Locate every uninfected red blood cell.
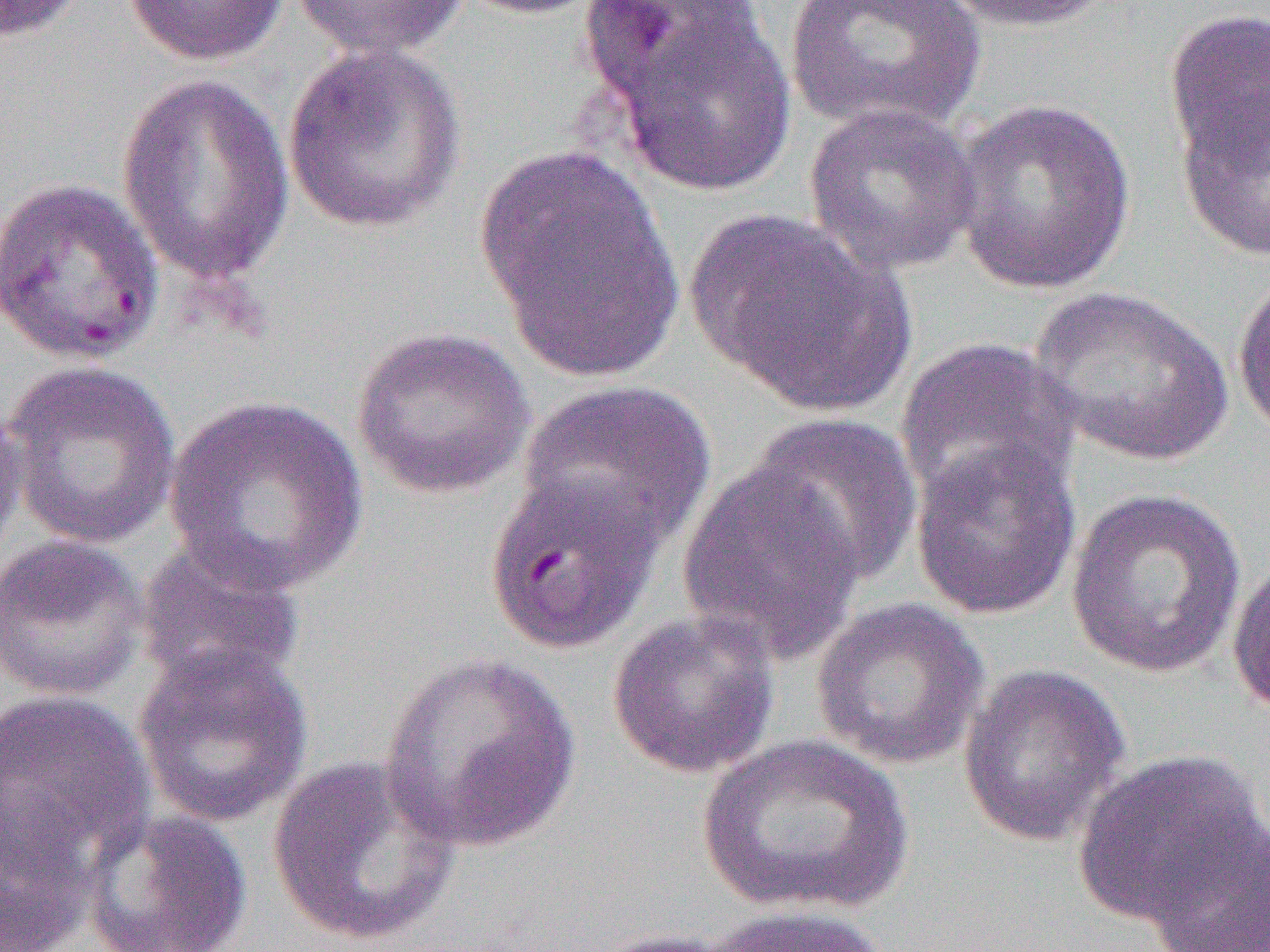

Approximate bounding boxes as named x1/y1/x2/y2 corners in pixels.
Uninfected red blood cells: (x1=0, y1=0, x2=92, y2=44), (x1=121, y1=0, x2=290, y2=66), (x1=292, y1=0, x2=469, y2=61), (x1=451, y1=0, x2=612, y2=19), (x1=782, y1=0, x2=987, y2=137), (x1=937, y1=0, x2=1119, y2=34), (x1=579, y1=1, x2=773, y2=104), (x1=591, y1=5, x2=799, y2=195), (x1=1163, y1=6, x2=1270, y2=192), (x1=283, y1=43, x2=467, y2=234), (x1=116, y1=73, x2=295, y2=287), (x1=1173, y1=77, x2=1270, y2=268), (x1=950, y1=98, x2=1137, y2=295), (x1=803, y1=101, x2=982, y2=275), (x1=476, y1=145, x2=683, y2=380), (x1=0, y1=176, x2=165, y2=365), (x1=686, y1=209, x2=908, y2=414), (x1=1233, y1=268, x2=1270, y2=444), (x1=1028, y1=285, x2=1234, y2=467), (x1=350, y1=326, x2=537, y2=500), (x1=894, y1=337, x2=1082, y2=511), (x1=2, y1=359, x2=181, y2=549), (x1=516, y1=377, x2=716, y2=554), (x1=163, y1=393, x2=369, y2=597), (x1=0, y1=395, x2=28, y2=567), (x1=746, y1=411, x2=924, y2=587), (x1=910, y1=436, x2=1081, y2=621), (x1=675, y1=459, x2=867, y2=666), (x1=483, y1=470, x2=664, y2=656), (x1=1065, y1=487, x2=1248, y2=680), (x1=0, y1=534, x2=149, y2=702), (x1=135, y1=536, x2=307, y2=698), (x1=1228, y1=552, x2=1270, y2=720), (x1=811, y1=597, x2=990, y2=769), (x1=607, y1=610, x2=781, y2=779), (x1=133, y1=645, x2=313, y2=828), (x1=378, y1=653, x2=585, y2=854), (x1=958, y1=661, x2=1131, y2=847), (x1=0, y1=689, x2=155, y2=871), (x1=695, y1=734, x2=916, y2=917), (x1=1071, y1=748, x2=1266, y2=929), (x1=267, y1=755, x2=462, y2=948), (x1=0, y1=791, x2=98, y2=952), (x1=79, y1=808, x2=253, y2=952), (x1=1144, y1=819, x2=1270, y2=952), (x1=703, y1=905, x2=896, y2=952), (x1=581, y1=928, x2=746, y2=952).

Summary:
  - Slide-level diagnosis: Plasmodium falciparum
  - Preparation: thin blood film
  - Image size: 1270×952 pixels
  - Modality: light microscopy
  - Field of view: single
  - Magnification: 1000x